Give the position of every Plasmodium parasite.
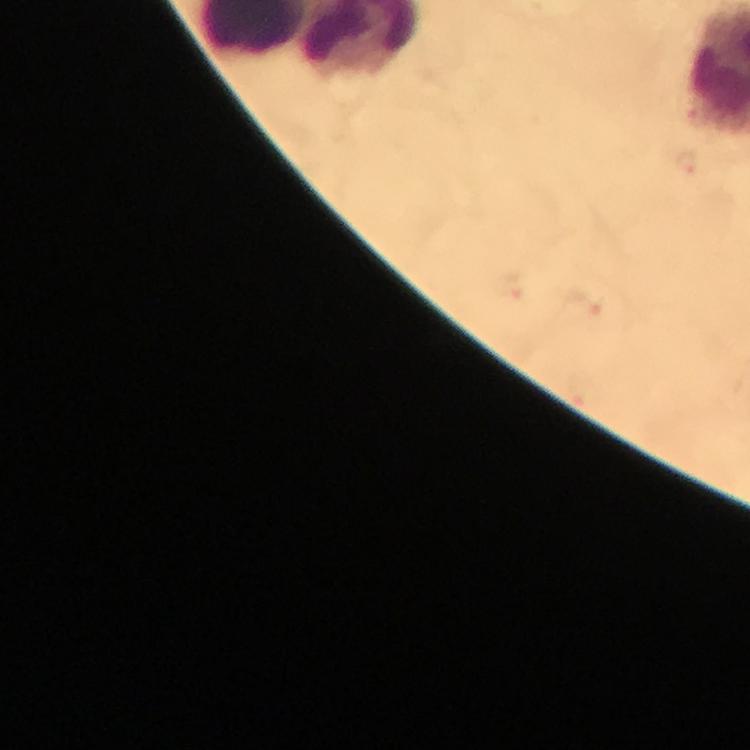

Approximate centers as [x, y] in pixels.
Plasmodium parasites: [688, 163], [583, 308].

image size = 750×750 pixels
magnification = 100x
stain = Giemsa
preparation = thick smear
capture = smartphone camera through the microscope
context = from a diagnostic examination for malaria
immersion oil = used
cropped from = a single field of view